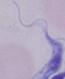 Captured at 1000x magnification. A trypanosome is shown. Micrograph.